Mark where cells are.
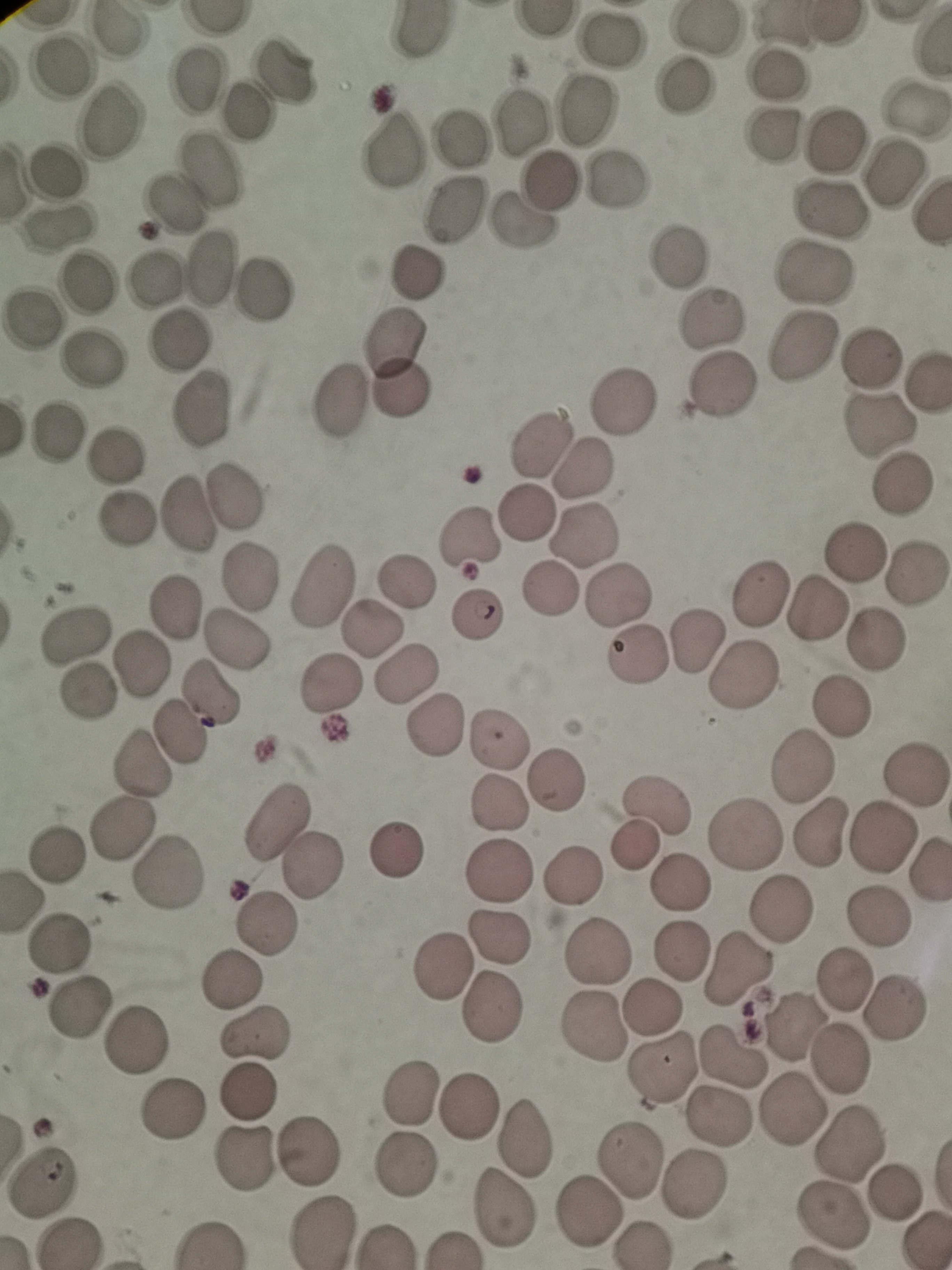

Approximate centers as [x, y] in pixels.
Cells: [114, 32], [611, 42], [59, 69], [286, 71], [779, 73], [195, 82], [685, 86], [914, 107], [580, 111], [247, 113], [516, 117], [106, 119], [770, 134], [461, 138], [835, 140], [391, 151], [209, 169], [51, 173], [892, 173], [546, 180], [618, 180], [172, 205], [830, 208], [456, 209], [930, 214], [518, 222], [58, 230], [677, 257], [209, 267], [819, 269], [156, 272], [417, 272], [86, 285], [263, 290], [712, 319], [34, 320], [177, 339], [396, 340], [800, 346], [873, 353], [89, 363], [925, 383], [724, 385], [399, 389], [338, 396], [621, 399], [202, 404], [882, 425], [53, 432], [539, 444], [117, 457], [586, 466], [907, 482], [233, 496], [183, 508], [527, 509], [123, 517], [584, 530], [469, 537], [856, 550], [248, 571], [917, 571], [407, 583], [552, 590], [757, 591], [620, 593], [175, 605], [817, 606], [475, 614], [372, 630], [71, 635], [235, 636], [696, 638], [871, 641], [638, 652], [141, 659], [407, 672], [744, 675], [331, 687], [90, 692], [210, 694], [840, 704], [435, 726], [180, 731], [498, 742], [144, 763], [801, 764], [915, 771], [557, 777], [496, 804], [658, 807], [273, 820], [122, 826], [745, 834], [820, 836], [887, 836], [635, 848], [397, 850], [55, 852], [497, 870], [310, 871], [168, 875], [572, 879], [681, 883], [781, 912], [879, 917], [265, 926], [498, 935], [60, 945], [684, 951], [595, 953], [441, 966], [735, 970], [844, 976], [233, 981], [77, 1009], [650, 1009], [491, 1011], [892, 1012], [795, 1026], [592, 1031], [255, 1037], [137, 1039], [734, 1058], [841, 1060], [660, 1067], [251, 1091], [411, 1091], [173, 1108], [789, 1108], [467, 1109], [720, 1120], [523, 1136], [852, 1142], [312, 1149], [242, 1159], [627, 1164], [406, 1168], [43, 1179], [694, 1185], [890, 1188], [502, 1207], [588, 1211], [828, 1216], [326, 1234].

{
  "field_of_view": "single",
  "preparation": "thin blood film",
  "image_size": "952×1270 pixels",
  "capture": "smartphone through the microscope eyepiece",
  "stain": "Giemsa"
}